State which parasite is depicted.
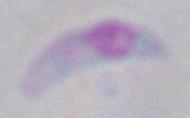
This is Toxoplasma gondii.

modality = micrograph
magnification = 1000x